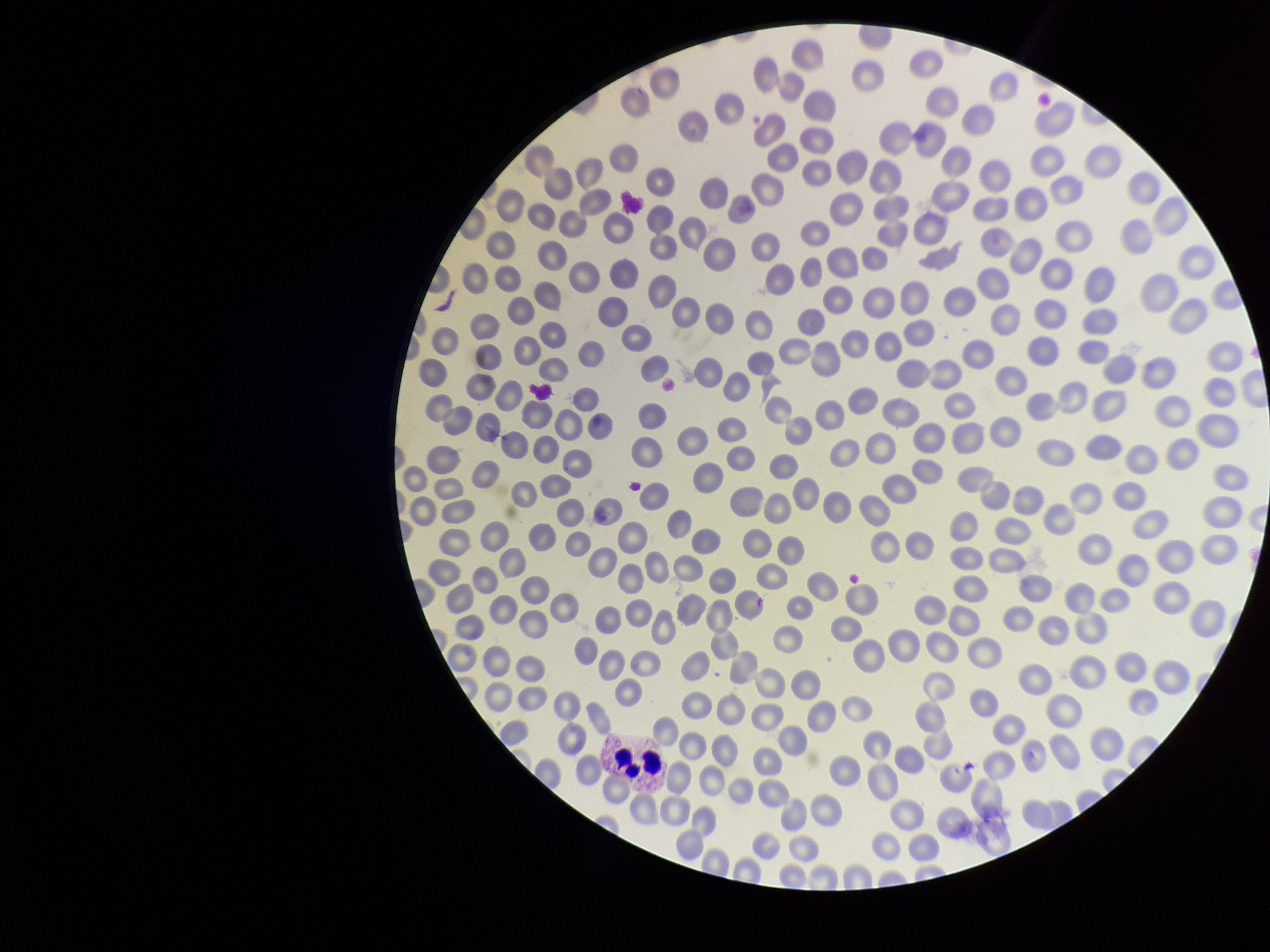
{
  "patient_malaria_status": "negative",
  "image_size": "1270×952 pixels",
  "parasitized_red_blood_cell_count": 0,
  "field_of_view": "one from this slide",
  "capture": "smartphone photograph through the microscope eyepiece",
  "red_blood_cell_count": 253,
  "parasitized_red_blood_cells": "none detected",
  "preparation": "thin smear",
  "stain": "Giemsa"
}